Outline each blood parasite and name the species.
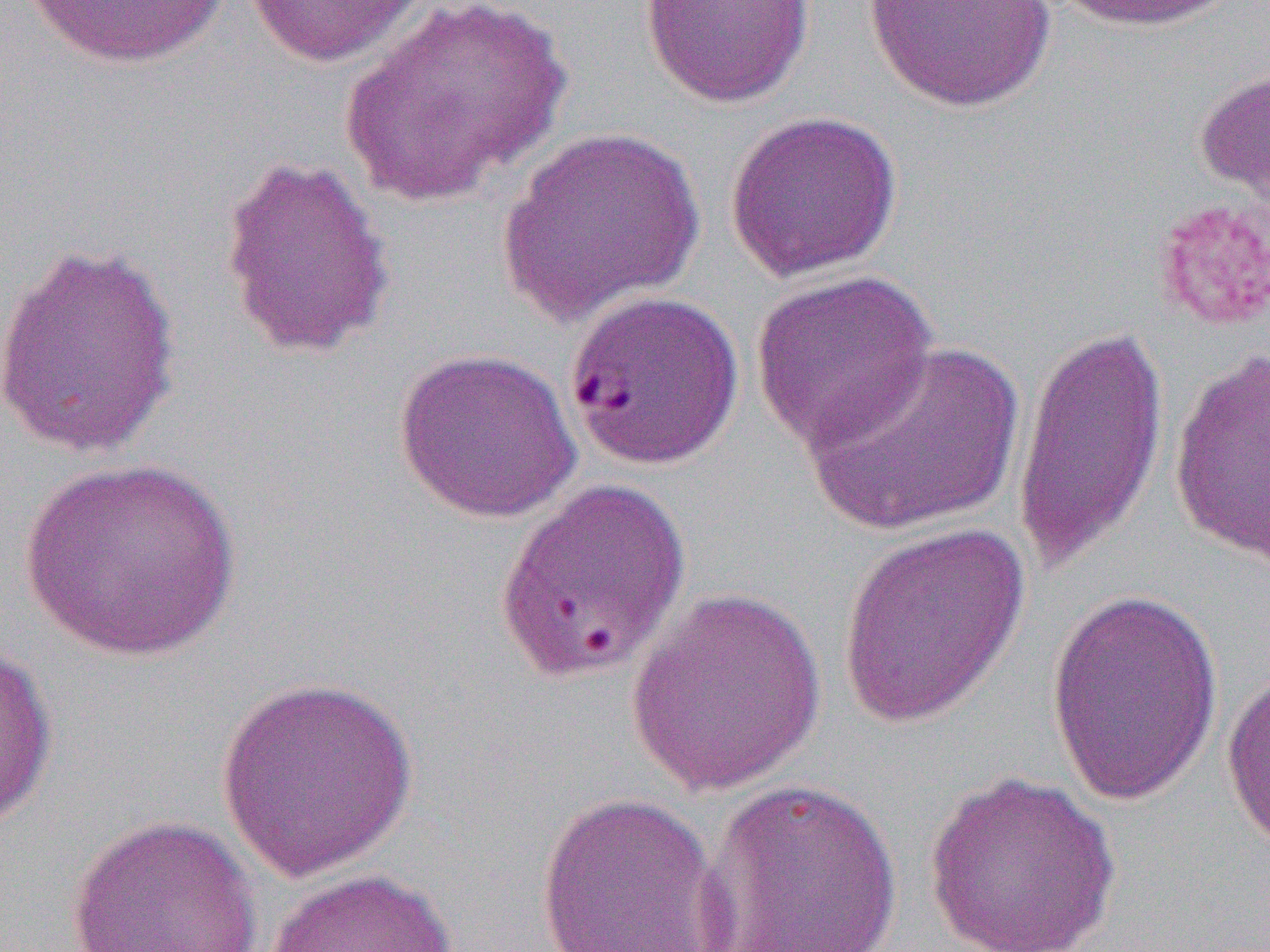
Approximate bounding boxes as (x1,y1)-(x2,y2) corner pairs in pixels.
Plasmodium falciparum-infected red blood cells (subset): (565,290)-(744,471).
No Plasmodium ovale, Plasmodium malariae, Plasmodium vivax, Babesia divergens, or Trypanosoma brucei observed.

Uninfected red blood cell locations (subset): (17,0)-(233,70), (339,0)-(571,207), (863,0)-(1058,113), (1051,0)-(1233,33), (240,1)-(430,68), (640,1)-(815,109), (1194,63)-(1270,214), (724,110)-(903,282), (496,126)-(704,327), (217,153)-(397,361), (0,238)-(183,462), (750,269)-(939,453), (1012,319)-(1170,582), (801,339)-(1027,538), (393,347)-(581,523), (1168,348)-(1270,569), (22,457)-(242,662), (837,523)-(1030,731), (623,587)-(827,796), (1045,587)-(1224,806), (0,638)-(58,829), (1221,664)-(1270,858), (216,674)-(420,883), (923,770)-(1122,950), (695,778)-(904,952), (534,790)-(732,952), (68,814)-(261,952), (264,866)-(460,952). Slide-level diagnosis: Plasmodium falciparum. Light microscopy. Thin blood smear. Image is 1270×952 pixels. Single field of view. Captured at 1000x magnification.